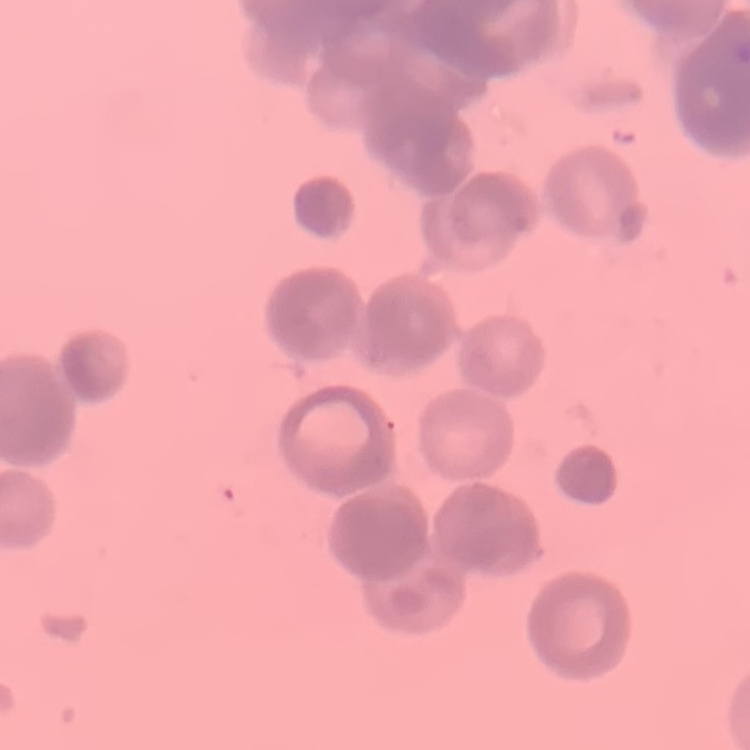
The erythrocytes exhibit rouleaux formation. Thin peripheral smear. Field's or Giemsa stain. One tile cut from a larger photomicrograph.